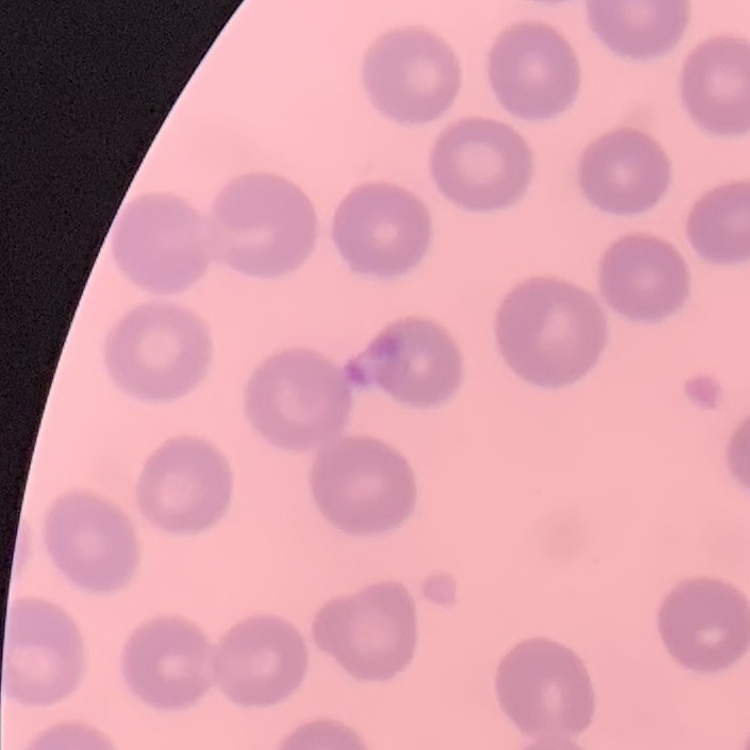
{
  "erythrocyte_morphology": "no rouleaux formation",
  "image_type": "one tile cut from a larger photomicrograph",
  "stain": "Field's or Giemsa",
  "preparation": "thin blood film"
}